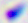
Summary:
  - Identification: Toxoplasma gondii
  - Modality: micrograph
  - Magnification: 400x